Comment on the morphology of the erythrocytes.
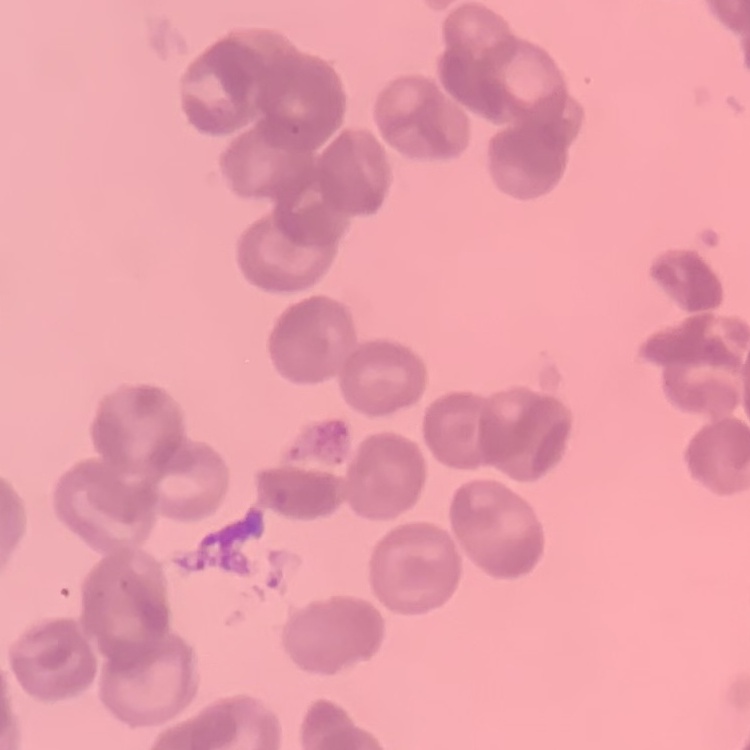
They show rouleaux formation.

stain = Field's or Giemsa
image type = one tile cut from a larger photomicrograph
preparation = thin peripheral smear